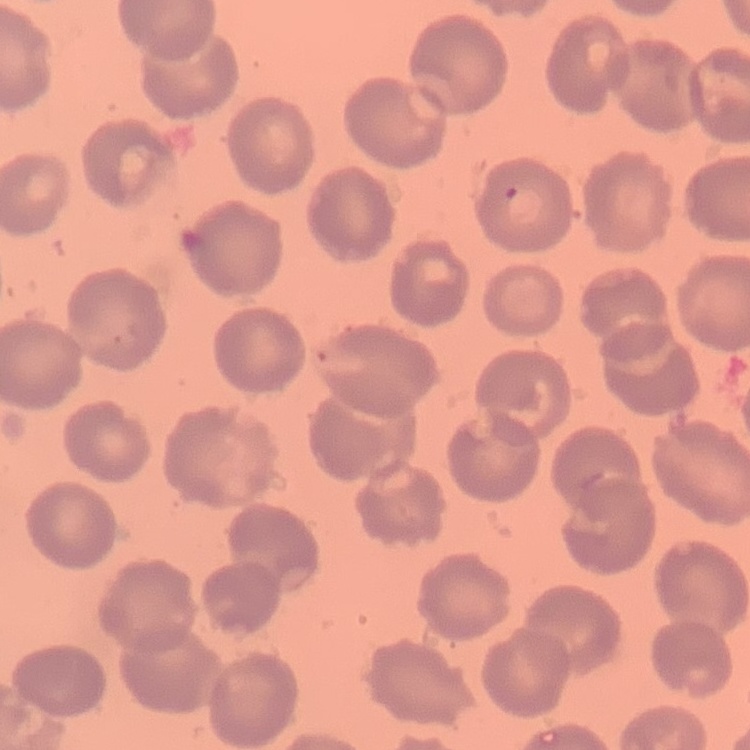 The erythrocytes show no rouleaux formation. Thin peripheral smear. Stained with either Field's or Giemsa. Square crop of a larger photomicrograph.